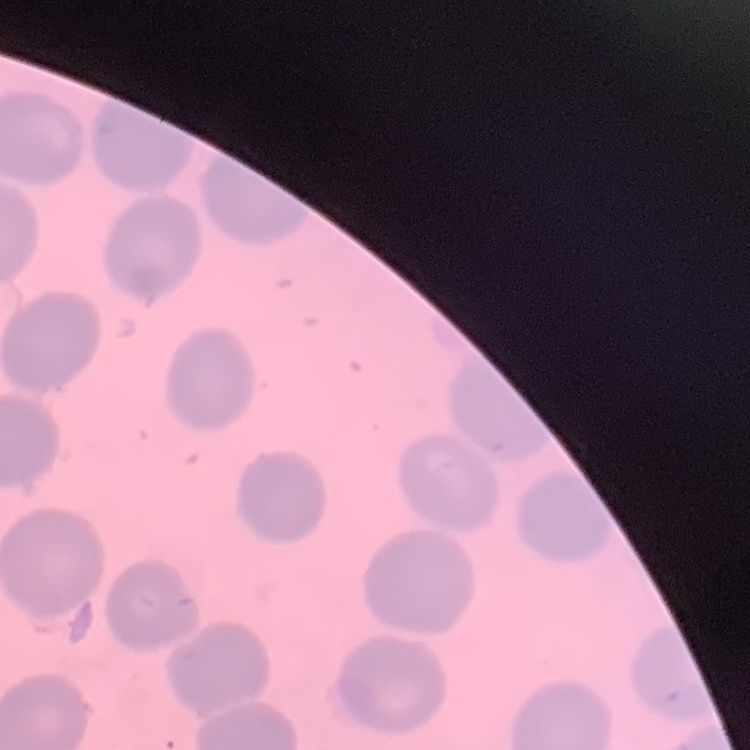
The red blood cells exhibit no rouleaux formation. Stained with either Field's or Giemsa. Thin blood film. Square crop of a larger photomicrograph.